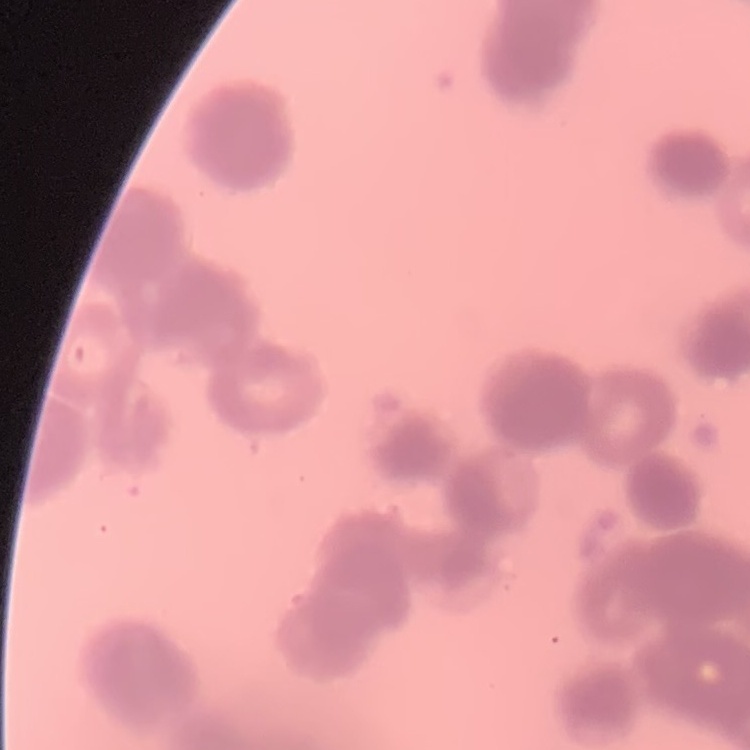
Summary:
  - Red blood cell morphology: rouleaux formation
  - Image type: one tile cut from a larger photomicrograph
  - Stain: Field's or Giemsa
  - Preparation: thin peripheral smear